Locate and identify every blood parasite.
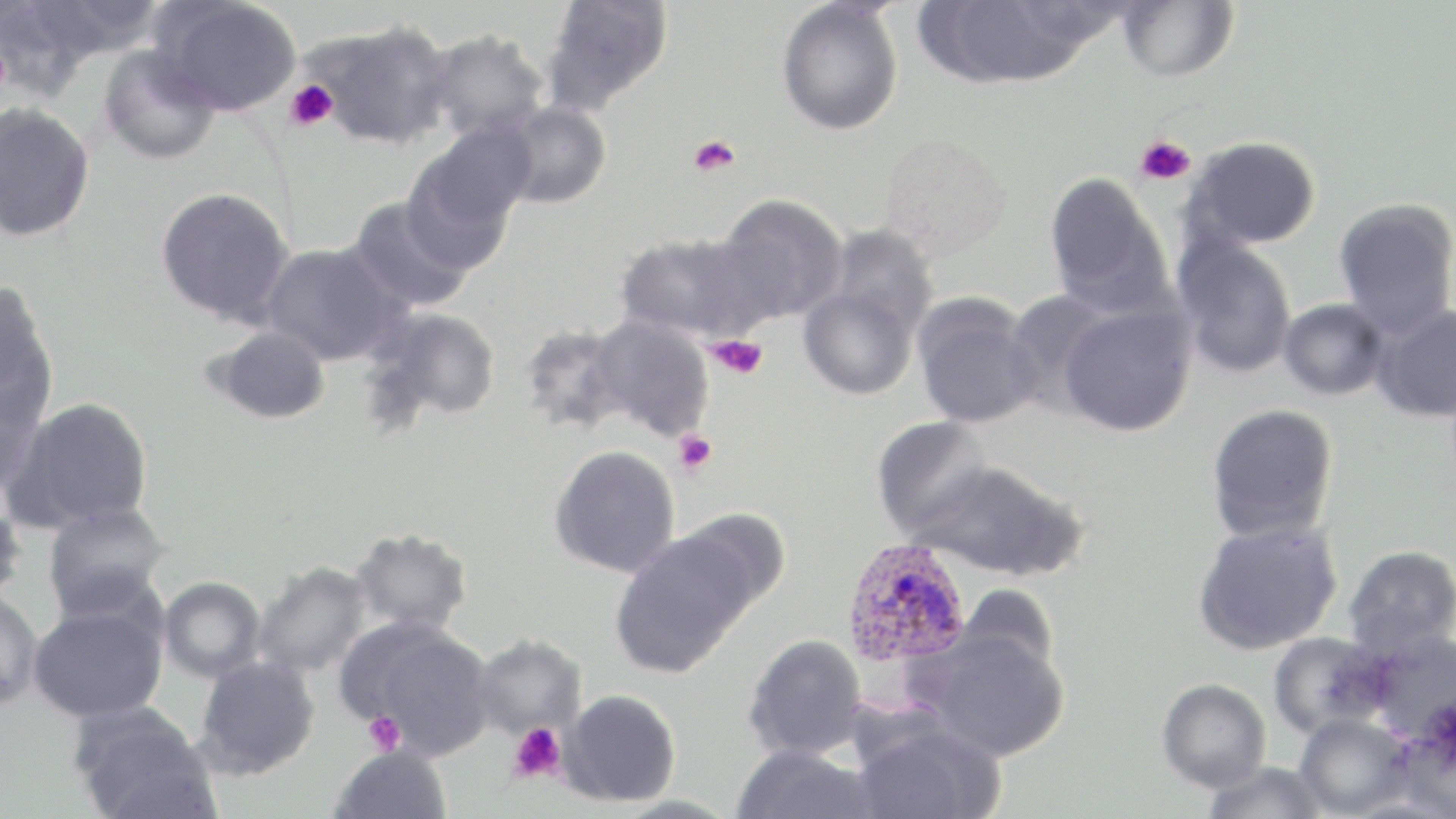
Approximate bounding boxes as named x1/y1/x2/y2 corners in pixels.
Plasmodium ovale-infected red blood cells: (x1=841, y1=539, x2=972, y2=671).
No Plasmodium falciparum, Plasmodium malariae, Plasmodium vivax, Babesia divergens, or Trypanosoma brucei observed.

slide-level diagnosis = Plasmodium ovale
uninfected red blood cell locations = approximate bounding boxes as named x1/y1/x2/y2 corners in pixels: (x1=20, y1=0, x2=167, y2=65), (x1=154, y1=0, x2=303, y2=117), (x1=540, y1=0, x2=674, y2=114), (x1=917, y1=0, x2=1106, y2=90), (x1=1117, y1=0, x2=1239, y2=83), (x1=776, y1=2, x2=904, y2=136), (x1=302, y1=19, x2=456, y2=151), (x1=425, y1=30, x2=552, y2=142), (x1=97, y1=45, x2=221, y2=166), (x1=494, y1=101, x2=612, y2=209), (x1=0, y1=102, x2=95, y2=242), (x1=407, y1=122, x2=536, y2=252), (x1=876, y1=132, x2=1013, y2=264), (x1=1184, y1=136, x2=1321, y2=251), (x1=1043, y1=170, x2=1173, y2=316), (x1=155, y1=186, x2=293, y2=325), (x1=714, y1=193, x2=849, y2=325), (x1=346, y1=197, x2=476, y2=314), (x1=1333, y1=197, x2=1456, y2=338), (x1=821, y1=225, x2=937, y2=344), (x1=614, y1=231, x2=767, y2=343), (x1=1171, y1=237, x2=1298, y2=379), (x1=259, y1=241, x2=402, y2=366), (x1=0, y1=280, x2=58, y2=424), (x1=797, y1=282, x2=920, y2=400), (x1=1002, y1=289, x2=1118, y2=417), (x1=912, y1=293, x2=1043, y2=429), (x1=1277, y1=298, x2=1391, y2=400), (x1=1057, y1=299, x2=1197, y2=437), (x1=1370, y1=302, x2=1456, y2=423), (x1=368, y1=307, x2=502, y2=423), (x1=586, y1=315, x2=716, y2=442), (x1=517, y1=322, x2=631, y2=435), (x1=209, y1=325, x2=331, y2=424), (x1=0, y1=378, x2=46, y2=500), (x1=6, y1=396, x2=154, y2=532), (x1=1206, y1=403, x2=1339, y2=544), (x1=871, y1=416, x2=996, y2=539), (x1=549, y1=445, x2=681, y2=578), (x1=912, y1=460, x2=1086, y2=581), (x1=0, y1=490, x2=27, y2=607), (x1=41, y1=501, x2=170, y2=618), (x1=676, y1=508, x2=792, y2=615), (x1=1193, y1=519, x2=1343, y2=656), (x1=350, y1=527, x2=473, y2=636), (x1=609, y1=530, x2=757, y2=679), (x1=1343, y1=545, x2=1456, y2=659), (x1=253, y1=561, x2=374, y2=678), (x1=158, y1=576, x2=266, y2=683), (x1=957, y1=584, x2=1059, y2=682), (x1=0, y1=589, x2=44, y2=710), (x1=28, y1=601, x2=168, y2=723), (x1=339, y1=617, x2=495, y2=758), (x1=917, y1=627, x2=1069, y2=761), (x1=1368, y1=629, x2=1456, y2=743), (x1=1267, y1=630, x2=1393, y2=739), (x1=743, y1=633, x2=869, y2=761), (x1=470, y1=635, x2=586, y2=740), (x1=195, y1=655, x2=320, y2=779), (x1=1157, y1=678, x2=1272, y2=793), (x1=558, y1=689, x2=681, y2=807), (x1=71, y1=705, x2=217, y2=819), (x1=1294, y1=713, x2=1415, y2=818), (x1=851, y1=718, x2=1006, y2=819), (x1=329, y1=743, x2=453, y2=819), (x1=730, y1=745, x2=879, y2=819), (x1=1201, y1=761, x2=1330, y2=819)
platelet locations = approximate bounding boxes as named x1/y1/x2/y2 corners in pixels: (x1=285, y1=81, x2=338, y2=132), (x1=1135, y1=134, x2=1197, y2=185), (x1=688, y1=135, x2=742, y2=177), (x1=705, y1=335, x2=768, y2=380), (x1=672, y1=430, x2=718, y2=477), (x1=363, y1=711, x2=406, y2=755), (x1=508, y1=723, x2=566, y2=784)
stain = May-Grünwald-Giemsa
modality = optical microscopy
field of view = one of a larger specimen
preparation = thin blood film
image size = 1456×819 pixels
magnification = 1000x